Point out every malaria parasite and every leukocyte.
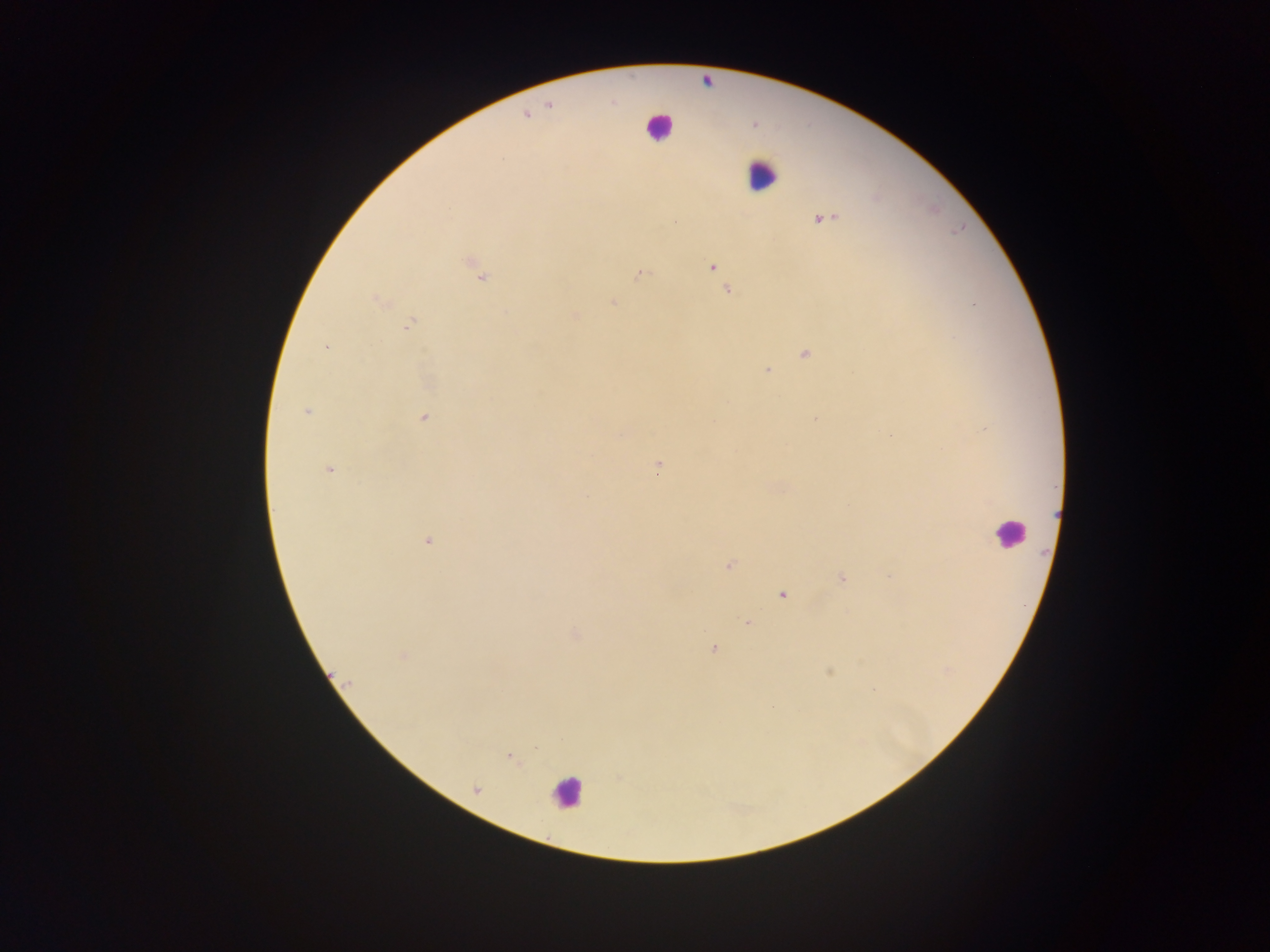
Approximate centers as {x, y} in pixels.
Malaria parasites: {549, 104}, {525, 115}, {820, 218}, {710, 264}, {640, 274}, {481, 275}, {726, 288}, {378, 298}, {614, 302}, {972, 304}, {575, 316}, {409, 324}, {326, 346}, {803, 354}, {766, 370}, {306, 409}, {423, 416}, {813, 417}, {620, 434}, {890, 435}, {657, 469}, {330, 470}, {428, 541}, {728, 564}, {889, 577}, {840, 579}, {782, 595}, {748, 623}, {575, 634}, {712, 647}, {402, 657}, {861, 664}, {828, 672}, {347, 681}, {873, 688}, {772, 708}, {510, 756}, {621, 778}.
Leukocytes: {662, 125}, {758, 180}, {1006, 533}, {566, 798}.

capture = mobile-phone photograph through a microscope
country = Ghana
field of view = single
preparation = thick blood film
image size = 1270×952 pixels